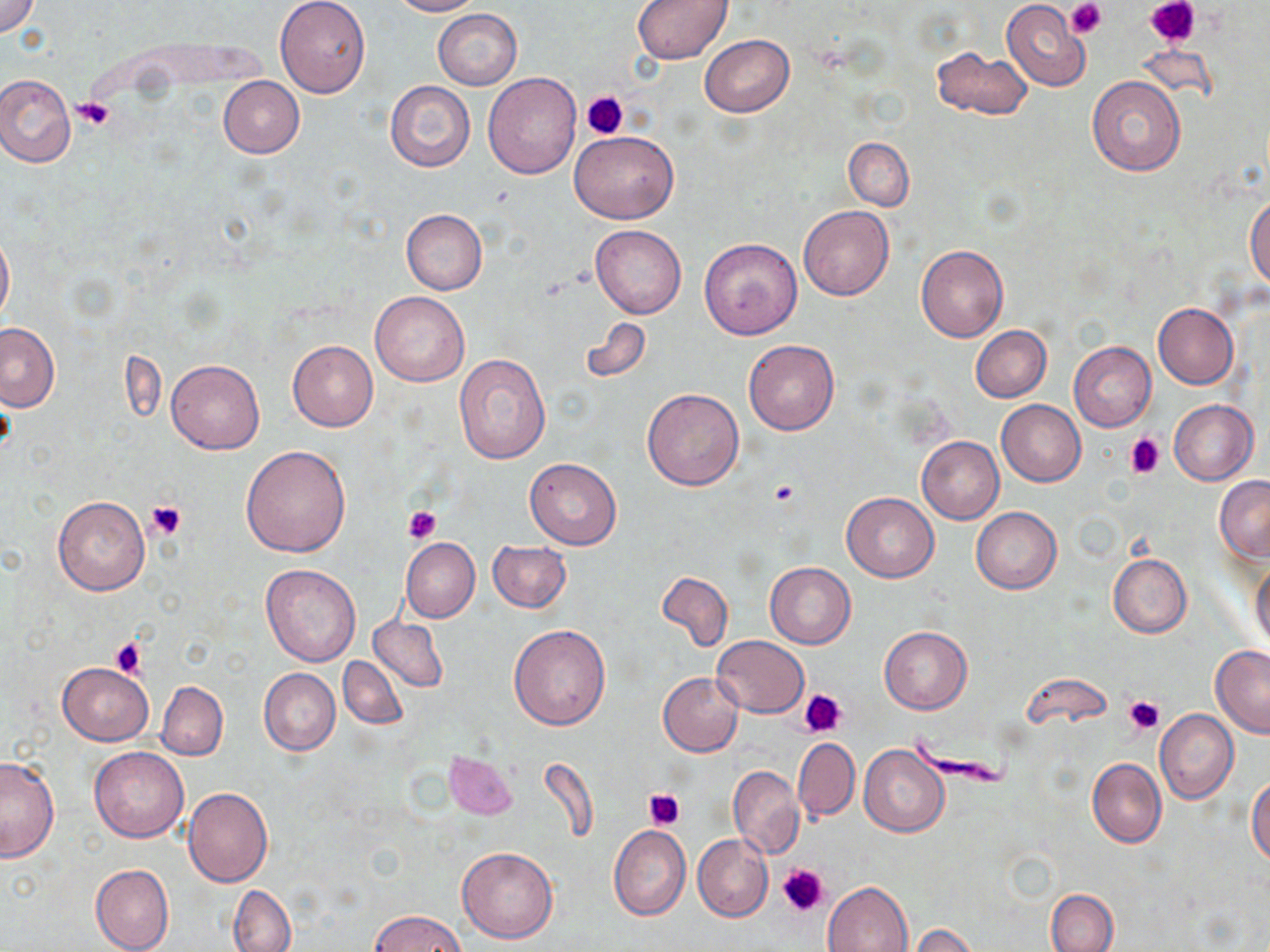 Approximate bounding boxes as [x1, y1, x2, y2] in pixels. Platelet locations: [1066, 0, 1106, 39], [1148, 0, 1199, 48], [581, 90, 628, 140], [73, 97, 116, 130], [1125, 432, 1166, 476], [769, 482, 799, 507], [144, 498, 189, 539], [405, 506, 441, 544], [112, 638, 145, 680], [801, 688, 848, 738], [1122, 695, 1164, 737], [643, 787, 687, 831], [775, 863, 829, 917]. Uninfected red blood cell locations: [0, 0, 41, 37], [275, 0, 371, 98], [390, 0, 482, 16], [632, 0, 733, 65], [1002, 0, 1091, 90], [434, 10, 521, 89], [700, 34, 794, 118], [932, 46, 1033, 121], [483, 72, 582, 178], [1, 73, 76, 167], [1086, 75, 1186, 176], [218, 76, 304, 158], [385, 81, 475, 171], [570, 130, 679, 224], [844, 138, 913, 210], [1246, 197, 1270, 290], [798, 206, 893, 301], [400, 208, 488, 295], [591, 225, 686, 318], [0, 229, 14, 327], [699, 238, 802, 340], [915, 244, 1009, 342], [369, 291, 469, 386], [1152, 303, 1238, 388], [580, 317, 652, 384], [0, 323, 59, 411], [971, 325, 1051, 402], [414, 332, 521, 465], [743, 338, 839, 435], [287, 339, 379, 431], [1069, 341, 1156, 431], [453, 353, 549, 462], [166, 359, 265, 454], [641, 388, 744, 491], [996, 400, 1086, 486], [1168, 400, 1258, 485], [916, 436, 1004, 525], [240, 445, 350, 558], [524, 458, 622, 549], [1215, 475, 1270, 561], [841, 492, 939, 581], [51, 493, 151, 596], [971, 506, 1061, 594], [401, 538, 480, 623], [487, 541, 571, 614], [1107, 553, 1191, 638], [1251, 561, 1269, 653], [765, 562, 856, 647], [261, 564, 361, 666], [655, 570, 734, 654], [368, 613, 449, 694], [508, 624, 612, 731], [879, 626, 972, 714], [711, 636, 809, 719], [1210, 646, 1270, 737], [338, 657, 408, 729], [56, 661, 154, 747], [282, 664, 403, 740], [258, 668, 340, 756], [658, 672, 743, 756], [157, 681, 228, 760], [1155, 710, 1239, 804], [793, 738, 859, 821], [859, 745, 949, 837], [90, 746, 188, 842], [443, 750, 520, 820], [0, 756, 60, 862], [1087, 757, 1165, 849], [728, 766, 803, 859], [1248, 776, 1270, 866], [182, 787, 272, 887], [608, 826, 691, 921], [693, 834, 773, 921], [457, 846, 558, 943], [90, 863, 174, 952], [823, 880, 913, 952], [228, 883, 295, 952], [1046, 889, 1119, 952], [369, 911, 469, 952], [907, 925, 979, 952]. Slide-level diagnosis: no evidence of blood parasites. Single field of view. Light microscopy. Thin blood smear. May-Grünwald-Giemsa stain. Image is 1270×952 pixels. Captured at 1000x magnification.